Classify this cell by malaria status.
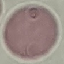

Uninfected.

preparation = thin smear
stain = Giemsa
image type = cell patch, automatically extracted from a larger field of view and resized to 64 × 64 pixels
capture = smartphone camera at the microscope eyepiece